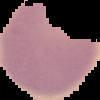 Result: negative for Plasmodium parasites. The area outside the segmented cell region is set to black. Image is 100×100 pixels. From a thin blood film.